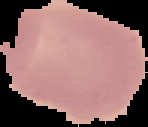 Malaria status: uninfected. From a thin blood smear. Image is 148×127 pixels. Cell region segmented out of the field of view; the surrounding area is masked to black.